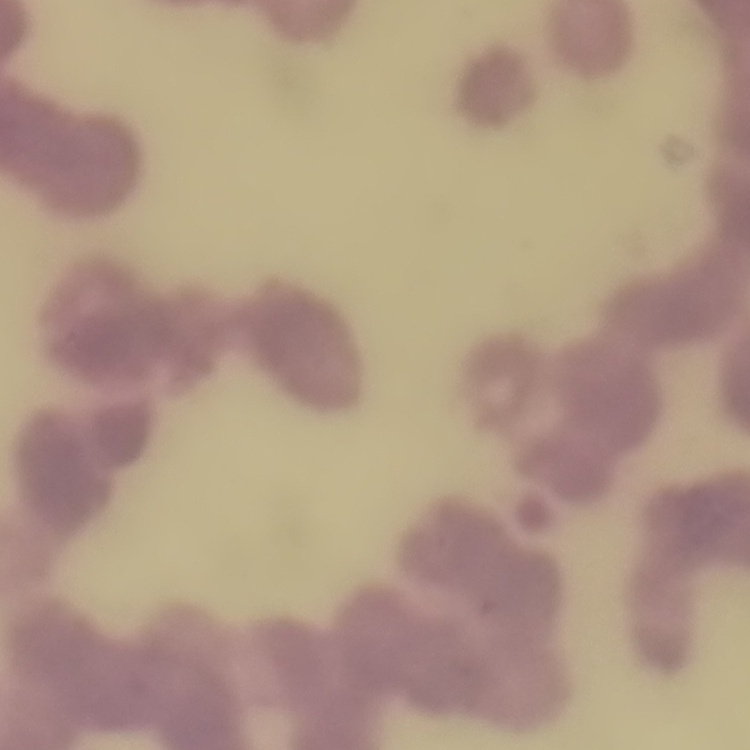 The red blood cells exhibit rouleaux formation. Square crop of a larger photomicrograph. Thin blood film. Field's or Giemsa stain.